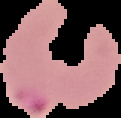

Summary:
  - Image type: segmented cell region with the area outside set to black
  - Image size: 121×118 pixels
  - Preparation: thin blood smear
  - Result: malaria parasites identified